Describe the morphology of the erythrocytes.
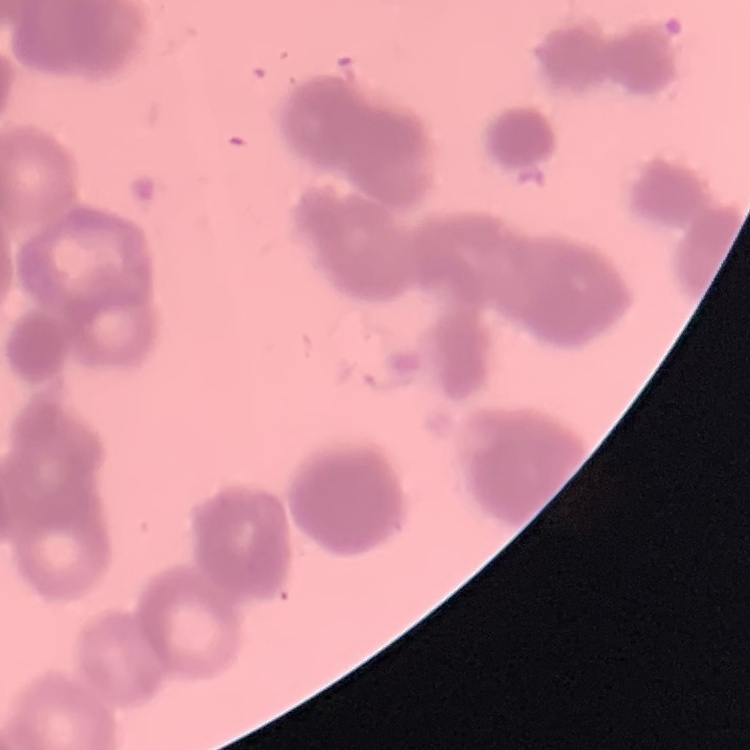
Rouleaux formation.

One tile cut from a larger photomicrograph. Thin blood film. Field's or Giemsa stain.